Comment on the morphology of the red blood cells.
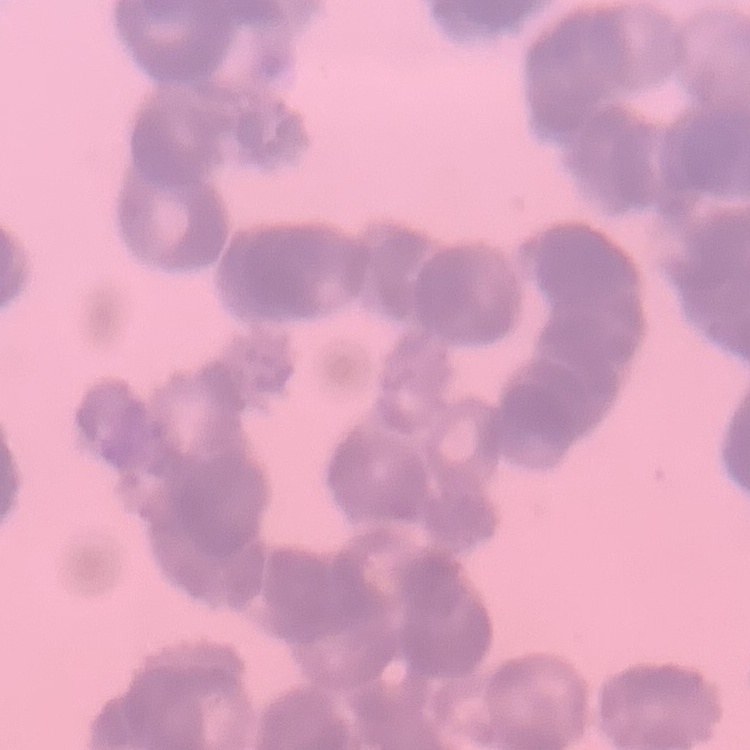

Rouleaux formation.

Field's or Giemsa stain. One tile cut from a larger photomicrograph. Thin blood smear.